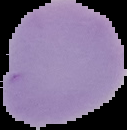
Summary:
  - Preparation: thin blood smear
  - Image type: cell region segmented out of the field of view; surrounding area masked to black
  - Malaria status: uninfected
  - Image size: 127×130 pixels